Describe the morphology of the red blood cells.
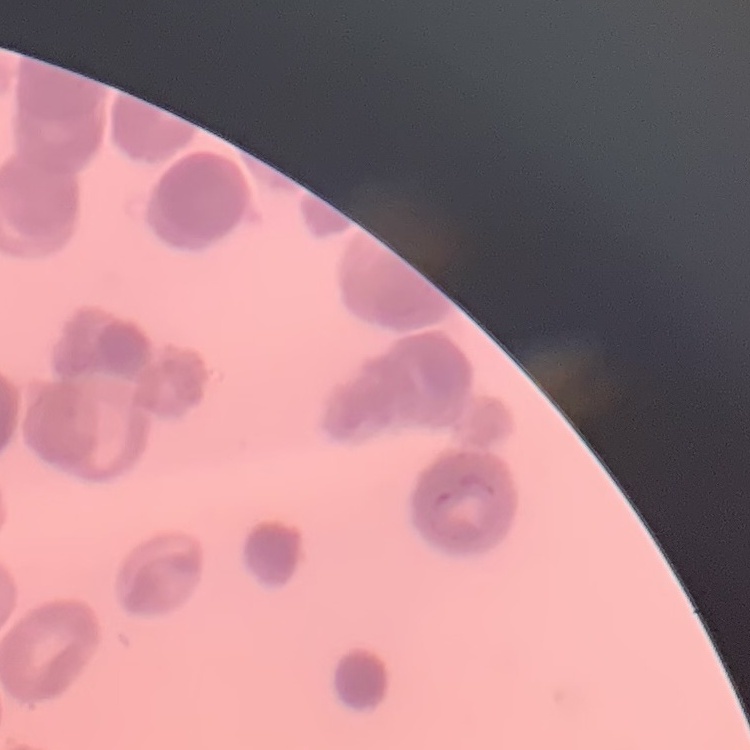

Rouleaux formation.

preparation: thin peripheral smear
image_type: square crop of a larger photomicrograph
stain: Field's or Giemsa